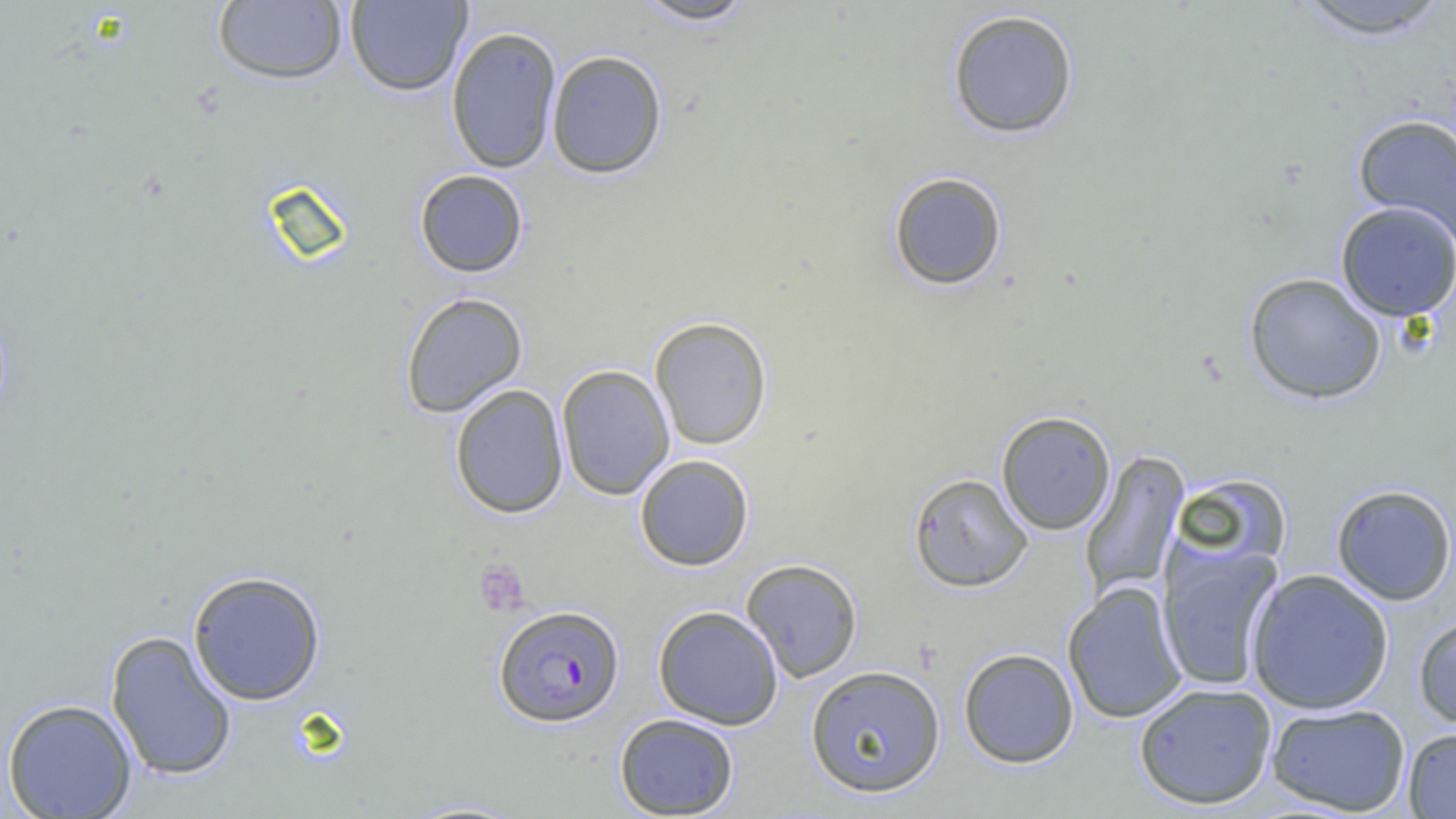

slide_level_diagnosis: Plasmodium falciparum
platelet_locations: 'approximate bounding boxes as (x1, y1, x2, y2) in pixels: (474, 560, 530, 616)'
field_of_view: one of a larger specimen
plasmodium_falciparum_infected_red_blood_cell_locations: 'approximate bounding boxes as (x1, y1, x2, y2) in pixels: (493, 604, 624, 727)'
modality: light microscopy
preparation: thin blood film
uninfected_red_blood_cell_locations: 'approximate bounding boxes as (x1, y1, x2, y2) in pixels: (345, 0, 472, 97), (632, 0, 759, 26), (1290, 0, 1455, 39), (212, 1, 348, 86), (946, 8, 1080, 139), (445, 25, 562, 174), (546, 50, 668, 179), (1352, 113, 1456, 247), (414, 169, 528, 278), (887, 171, 1008, 291), (1335, 201, 1456, 322), (1244, 272, 1387, 405), (400, 292, 528, 417), (649, 316, 773, 450), (556, 364, 675, 500), (449, 384, 569, 519), (996, 410, 1116, 535), (1080, 450, 1189, 601), (634, 454, 754, 571), (908, 472, 1033, 592), (1172, 473, 1292, 569), (1330, 483, 1456, 605), (1157, 543, 1283, 692), (741, 558, 863, 682), (1245, 568, 1394, 714), (188, 570, 327, 705), (1062, 582, 1187, 724), (653, 605, 784, 730), (1413, 613, 1456, 731), (105, 630, 237, 781), (958, 648, 1079, 768), (805, 664, 947, 798), (1134, 682, 1278, 810), (1, 697, 137, 818), (1265, 702, 1411, 816), (614, 712, 740, 818), (1402, 727, 1456, 818), (394, 798, 534, 818)'
image_size: 1456×819 pixels
magnification: 1000x